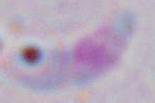 Micrograph. Toxoplasma gondii is shown. Captured at 1000x magnification.